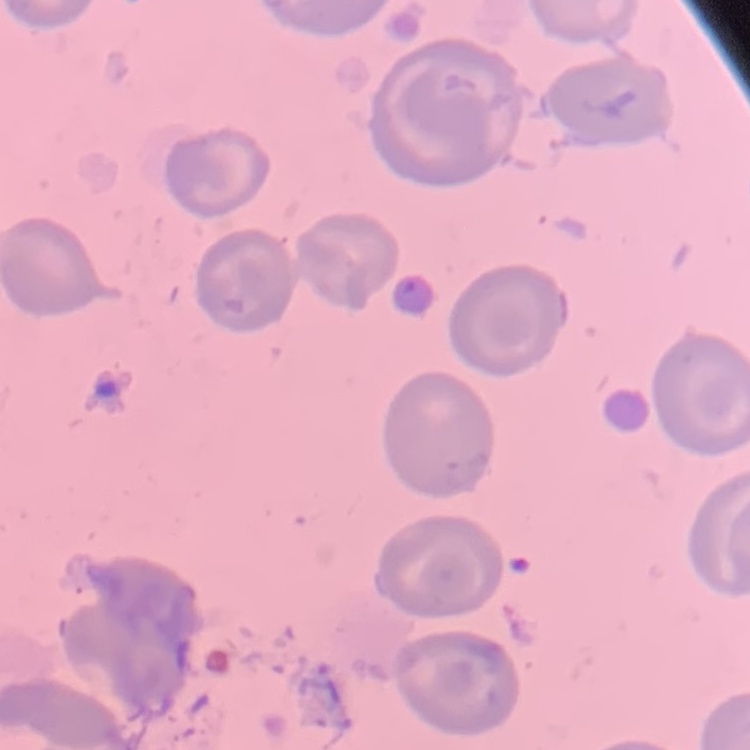

The red blood cells exhibit no rouleaux formation. Stained with either Field's or Giemsa. Thin blood smear. Square crop of a larger photomicrograph.